Outline each blood parasite and name the species.
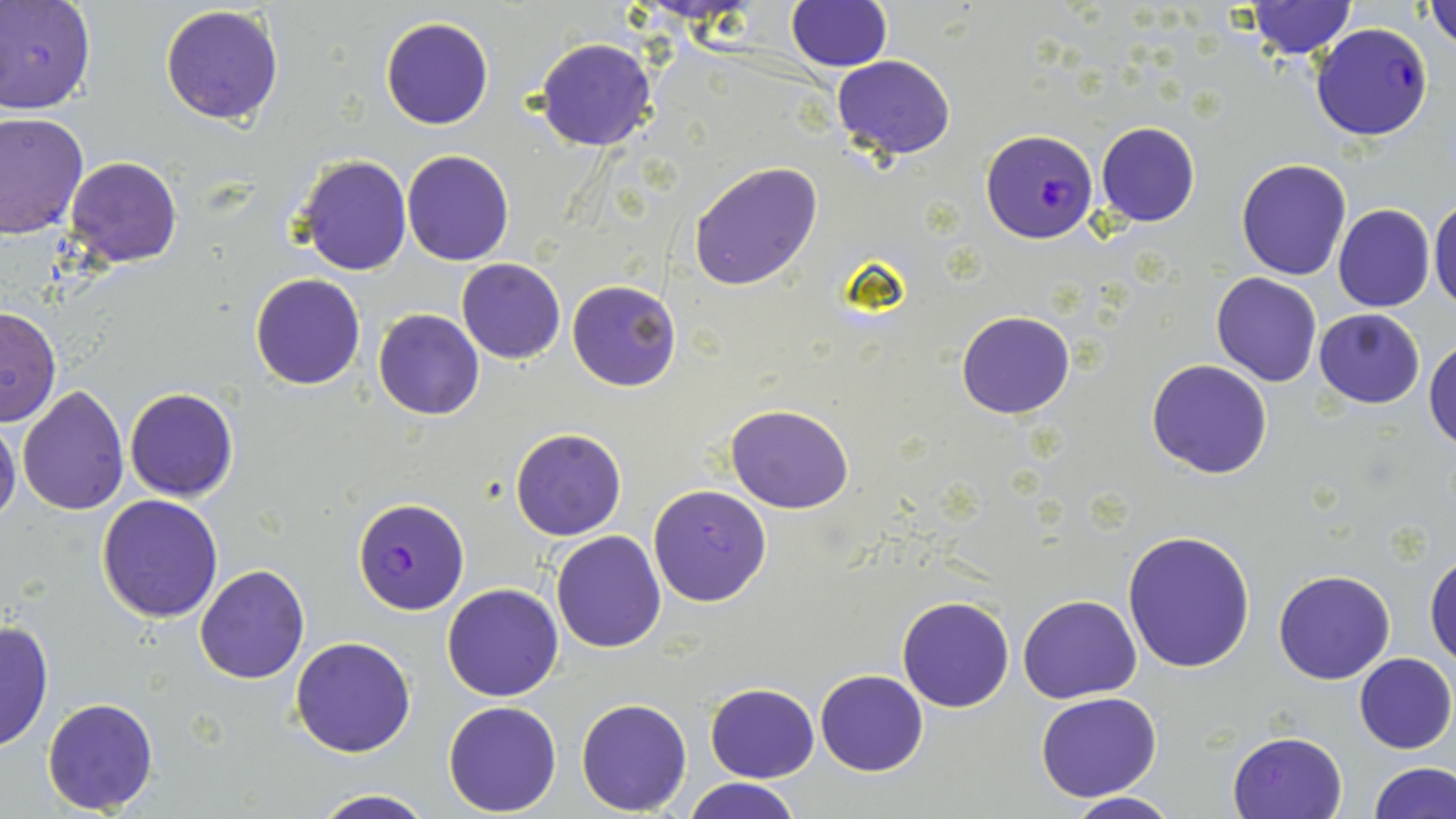
Approximate bounding boxes as (x1,y1)-(x2,y2) corner pairs in pixels.
Plasmodium falciparum-infected red blood cells: (1310,22)-(1434,141), (982,128)-(1097,244), (352,497)-(471,615).
No Plasmodium ovale, Plasmodium malariae, Plasmodium vivax, Babesia divergens, or Trypanosoma brucei observed.

Uninfected red blood cell locations: (1425,0)-(1456,49), (0,1)-(97,115), (787,1)-(892,71), (1243,2)-(1356,58), (159,4)-(285,126), (380,17)-(492,131), (534,37)-(658,151), (831,54)-(955,158), (1,113)-(90,241), (1095,121)-(1200,228), (401,148)-(515,266), (294,154)-(412,275), (64,156)-(183,267), (1236,158)-(1353,280), (688,161)-(823,290), (1429,196)-(1456,313), (1333,204)-(1435,313), (455,257)-(566,363), (1210,272)-(1322,387), (249,274)-(366,389), (567,279)-(682,391), (0,302)-(62,429), (373,308)-(484,421), (1315,308)-(1425,409), (955,311)-(1074,420), (1425,338)-(1456,450), (1146,359)-(1274,478), (18,382)-(129,515), (123,387)-(239,503), (725,405)-(854,513), (0,415)-(22,529), (511,428)-(627,540), (648,484)-(773,607), (96,494)-(225,622), (1122,529)-(1258,673), (550,530)-(665,653), (1425,551)-(1456,668), (193,565)-(309,684), (1273,569)-(1394,685), (442,582)-(564,702), (1018,593)-(1142,703), (897,595)-(1015,712), (0,622)-(53,754), (291,636)-(416,757), (1354,653)-(1456,753), (814,669)-(928,776), (704,683)-(818,782), (1035,692)-(1163,803), (42,696)-(160,813), (574,697)-(693,815), (443,701)-(563,816), (1228,732)-(1348,819), (1368,763)-(1455,818), (681,777)-(802,819), (305,790)-(441,819), (1063,792)-(1180,819). Slide-level diagnosis: Plasmodium falciparum. One field of a larger specimen. Thin blood smear. Light microscopy. May-Grünwald-Giemsa stain. Captured at 1000x magnification. Image is 1456×819 pixels.